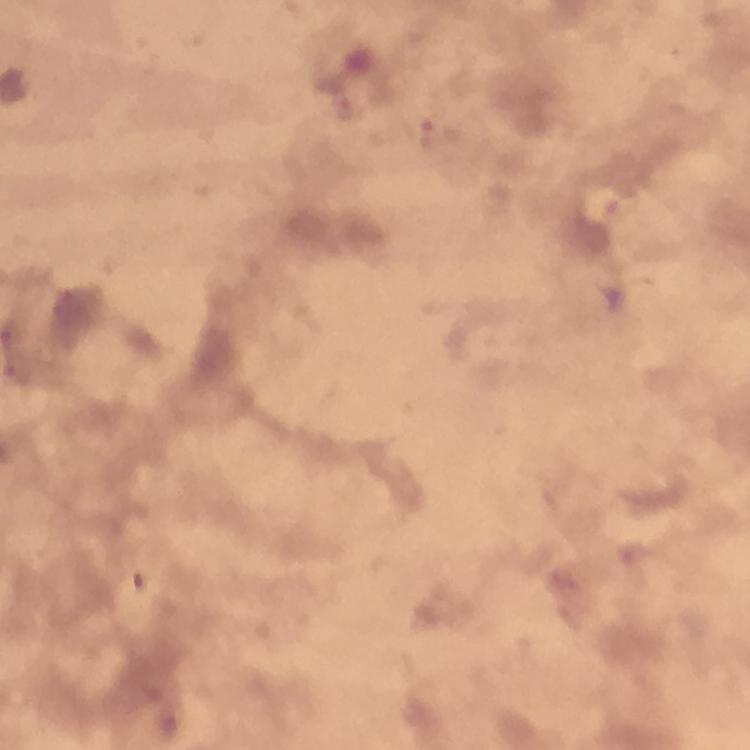
Approximate object centers, in pixels from the top-left corner.
Summary:
  - Plasmodium parasite locations: (x=437, y=135), (x=140, y=582), (x=167, y=725)
  - Context: from a malaria diagnostic workup
  - Preparation: thick blood film
  - Image size: 750×750 pixels
  - Magnification: 100x
  - Immersion oil: used
  - Cropped from: one field of view
  - Capture: smartphone camera through the microscope
  - Stain: Giemsa